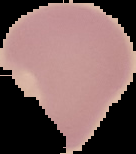

{
  "preparation": "thin blood smear",
  "image_type": "segmented cell region with the area outside set to black",
  "result": "negative for malaria parasites",
  "image_size": "136×154 pixels"
}